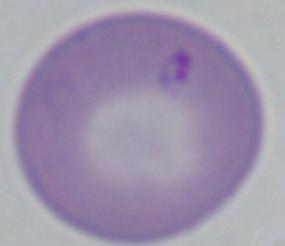
modality = micrograph
magnification = 1000x
identification = Babesia